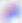

Summary:
  - Identification: Toxoplasma gondii
  - Modality: photomicrograph
  - Magnification: 400x